Report the malaria status of this cell.
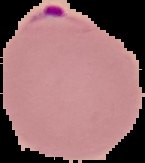

Parasitized.

Summary:
  - Image type: cell region segmented out of the field of view; surrounding area masked to black
  - Image size: 145×163 pixels
  - Preparation: thin blood smear